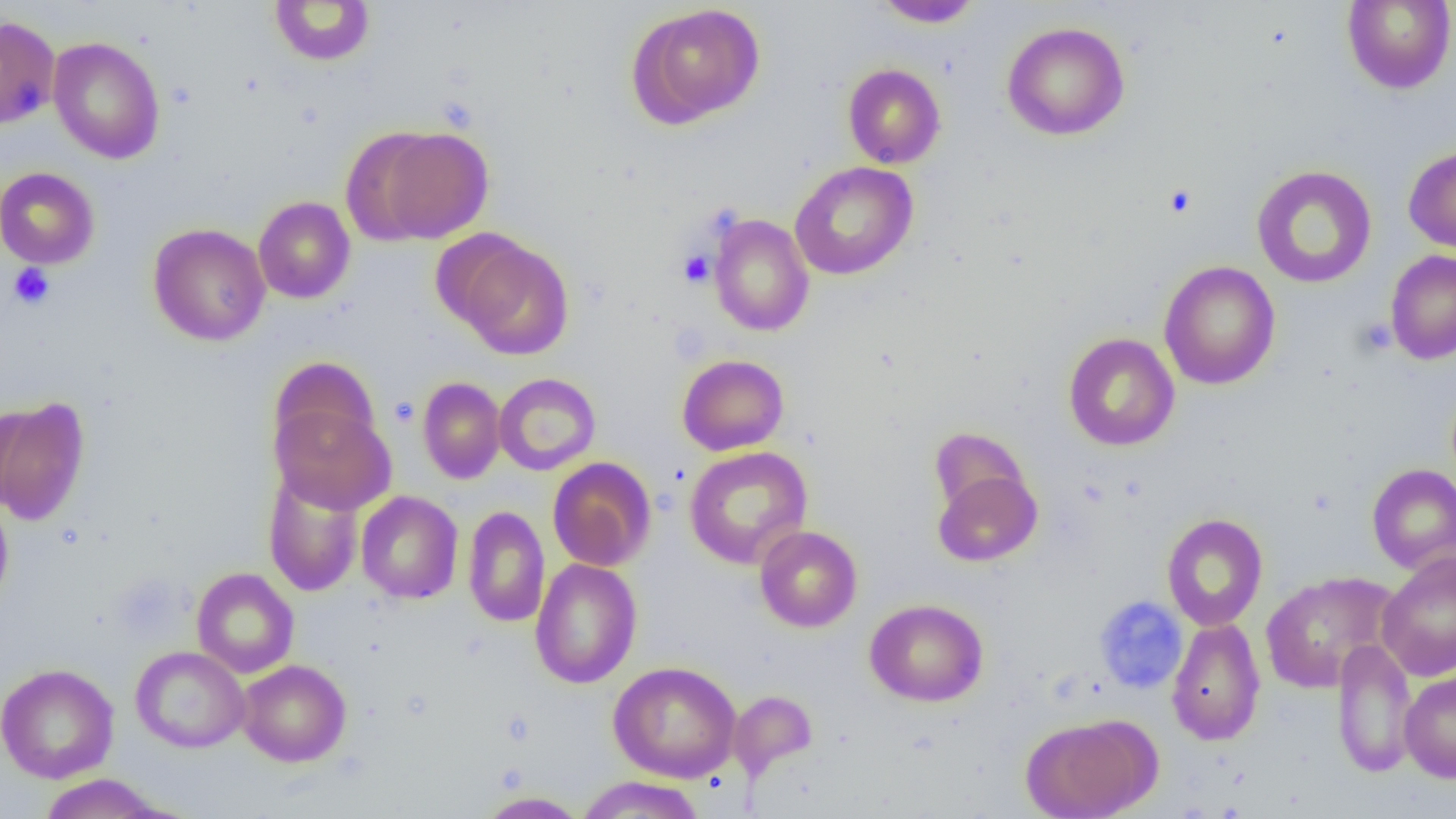
Summary:
  - Coordinate format: approximate bounding boxes as named x1/y1/x2/y2 corners in pixels
  - Uninfected red blood cell locations: (x1=874, y1=0, x2=982, y2=28), (x1=269, y1=1, x2=376, y2=66), (x1=1342, y1=1, x2=1456, y2=94), (x1=629, y1=3, x2=766, y2=127), (x1=0, y1=15, x2=61, y2=130), (x1=1002, y1=21, x2=1130, y2=141), (x1=48, y1=36, x2=165, y2=164), (x1=843, y1=63, x2=946, y2=168), (x1=367, y1=125, x2=495, y2=243), (x1=1403, y1=145, x2=1456, y2=254), (x1=789, y1=161, x2=918, y2=280), (x1=1251, y1=165, x2=1377, y2=288), (x1=0, y1=167, x2=100, y2=269), (x1=253, y1=196, x2=355, y2=304), (x1=709, y1=214, x2=814, y2=336), (x1=148, y1=223, x2=270, y2=346), (x1=450, y1=236, x2=574, y2=361), (x1=1385, y1=249, x2=1456, y2=365), (x1=1159, y1=261, x2=1281, y2=390), (x1=1063, y1=332, x2=1179, y2=451), (x1=677, y1=354, x2=789, y2=456), (x1=268, y1=356, x2=380, y2=461), (x1=494, y1=372, x2=601, y2=475), (x1=418, y1=376, x2=506, y2=484), (x1=0, y1=396, x2=90, y2=526), (x1=271, y1=400, x2=396, y2=515), (x1=929, y1=426, x2=1030, y2=519), (x1=684, y1=446, x2=812, y2=569), (x1=548, y1=457, x2=656, y2=571), (x1=1367, y1=463, x2=1456, y2=575), (x1=932, y1=467, x2=1042, y2=567), (x1=263, y1=470, x2=365, y2=597), (x1=356, y1=490, x2=464, y2=604), (x1=0, y1=494, x2=14, y2=610), (x1=462, y1=506, x2=549, y2=627), (x1=1161, y1=513, x2=1268, y2=631), (x1=754, y1=525, x2=862, y2=632), (x1=1377, y1=552, x2=1456, y2=681), (x1=529, y1=558, x2=643, y2=689), (x1=191, y1=567, x2=300, y2=678), (x1=1259, y1=571, x2=1400, y2=694), (x1=864, y1=598, x2=989, y2=707), (x1=1167, y1=617, x2=1266, y2=746), (x1=1330, y1=638, x2=1418, y2=778), (x1=131, y1=646, x2=249, y2=752), (x1=237, y1=659, x2=351, y2=767), (x1=608, y1=660, x2=742, y2=783), (x1=0, y1=663, x2=119, y2=783), (x1=1399, y1=672, x2=1456, y2=782), (x1=728, y1=690, x2=818, y2=781), (x1=1020, y1=714, x2=1158, y2=819), (x1=38, y1=774, x2=167, y2=818), (x1=576, y1=775, x2=705, y2=819), (x1=477, y1=791, x2=590, y2=818)
  - Platelet locations: (x1=1163, y1=184, x2=1197, y2=218), (x1=679, y1=250, x2=715, y2=287), (x1=8, y1=263, x2=55, y2=309), (x1=390, y1=397, x2=419, y2=427)
  - Slide-level diagnosis: negative for blood parasites
  - Preparation: thin blood smear
  - Image size: 1456×819 pixels
  - Modality: light microscopy
  - Field of view: one of a larger specimen
  - Magnification: 1000x